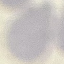 Result: negative for malaria parasites. Thin blood smear. Giemsa-stained preparation. Photographed with a smartphone camera at the microscope eyepiece. Automatically extracted cell patch, resized to 64 × 64 pixels.